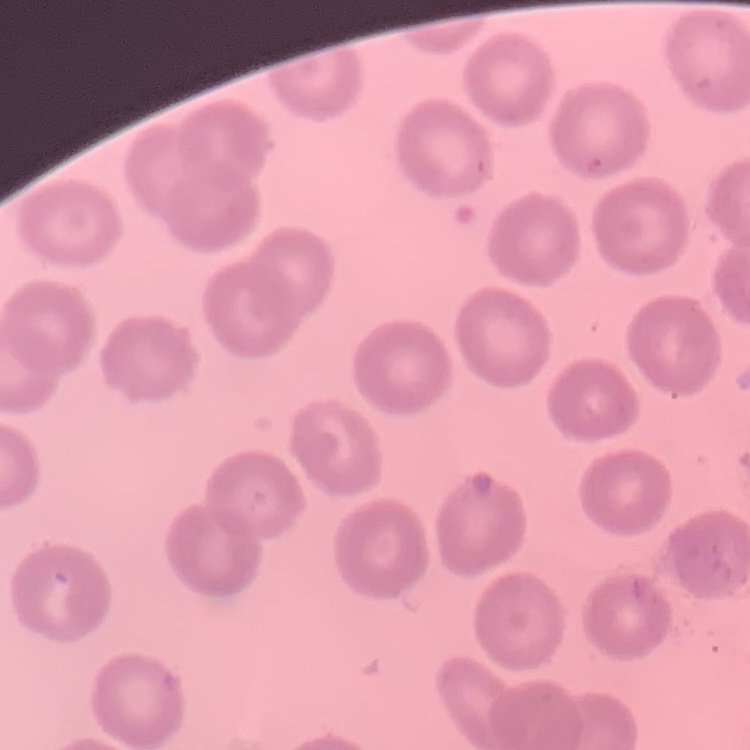
The erythrocytes show no rouleaux formation. Thin peripheral smear. Field's or Giemsa stain. One tile cut from a larger photomicrograph.